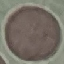
malaria status = uninfected
stain = Giemsa
image type = cell patch, automatically extracted from a larger field of view and resized to 64 × 64 pixels
capture = smartphone camera at the microscope eyepiece
preparation = thin blood smear